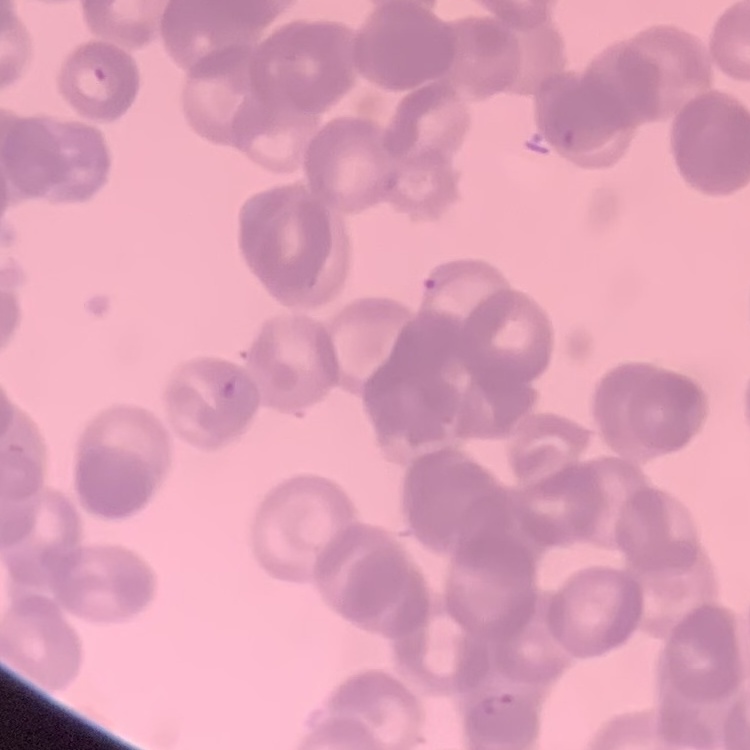

erythrocyte morphology = rouleaux formation
stain = Field's or Giemsa
preparation = thin peripheral smear
image type = square crop of a larger photomicrograph